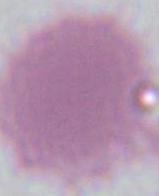
Summary:
  - Magnification: 1000x
  - Modality: micrograph
  - Identification: red blood cell